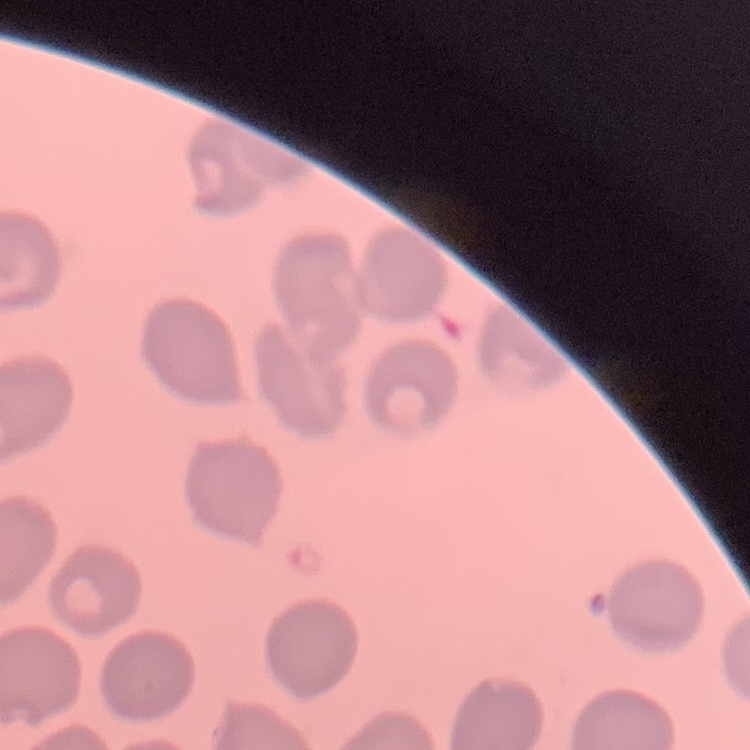
Summary:
  - Erythrocyte morphology: no rouleaux formation
  - Stain: Field's or Giemsa
  - Image type: one tile cut from a larger photomicrograph
  - Preparation: thin peripheral smear